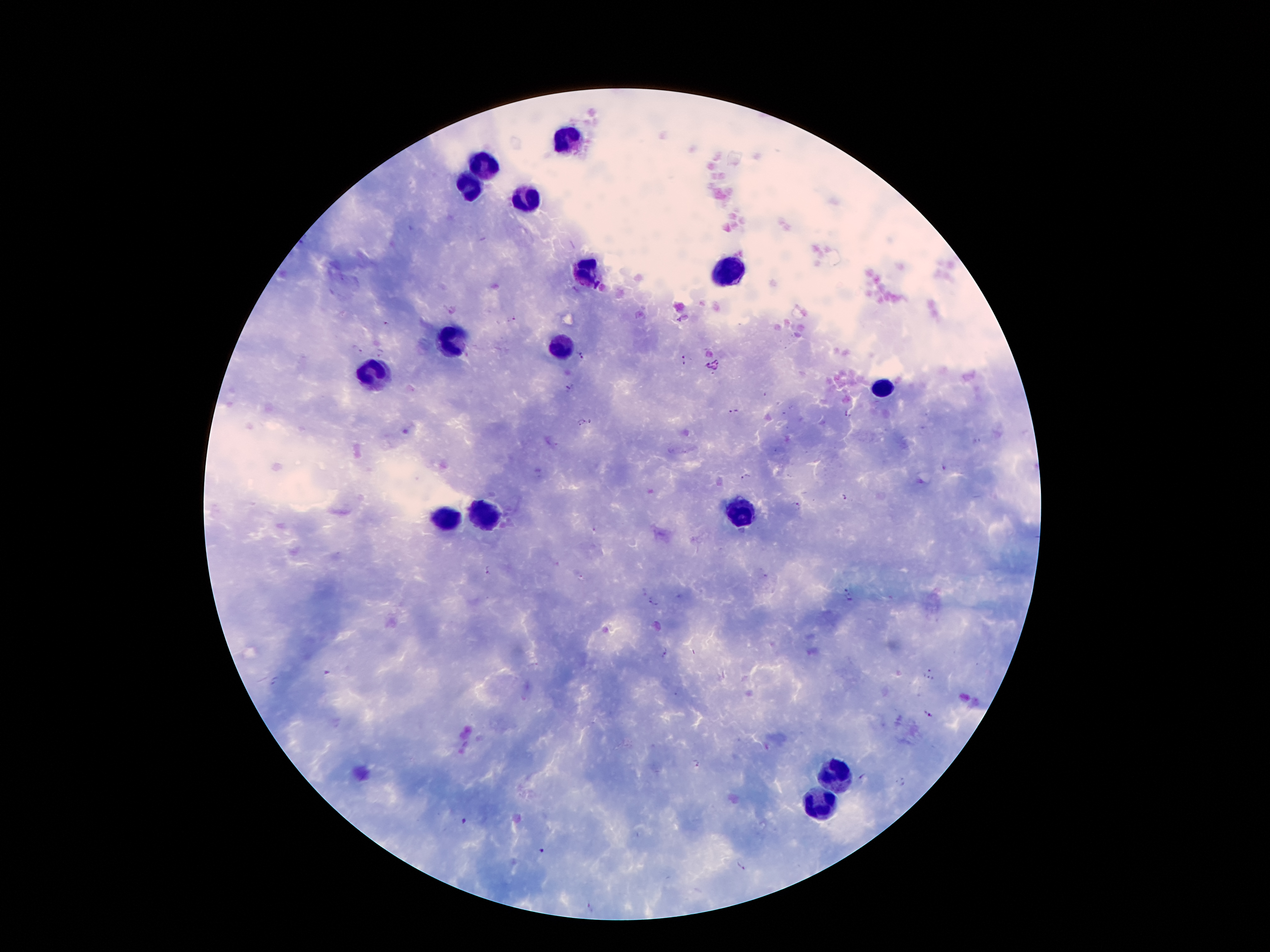
Approximate centers as (x, y) in pixels. Leukocyte locations: (568, 136), (484, 167), (469, 188), (525, 202), (726, 269), (584, 272), (451, 341), (561, 349), (376, 379), (882, 390), (483, 512), (738, 512), (449, 521), (829, 775), (822, 799). Plasmodium parasite locations: (452, 309), (512, 320), (386, 324), (357, 349), (380, 353), (581, 355), (685, 359), (570, 388), (734, 411), (848, 414), (581, 422), (591, 422), (944, 470), (745, 476), (844, 497), (796, 504), (594, 530), (486, 570), (765, 576), (581, 578), (844, 589), (644, 592), (848, 598), (652, 602), (666, 653), (931, 670), (325, 672), (928, 679), (274, 681), (928, 715), (698, 764), (862, 776), (902, 782), (464, 821), (542, 850), (741, 866), (590, 907). Patient malaria status: infected with Plasmodium falciparum. Smartphone photograph taken through the microscope eyepiece. Thick peripheral-blood smear. Image is 1270×952 pixels. Single field of view. Giemsa-stained preparation. 100x magnification.